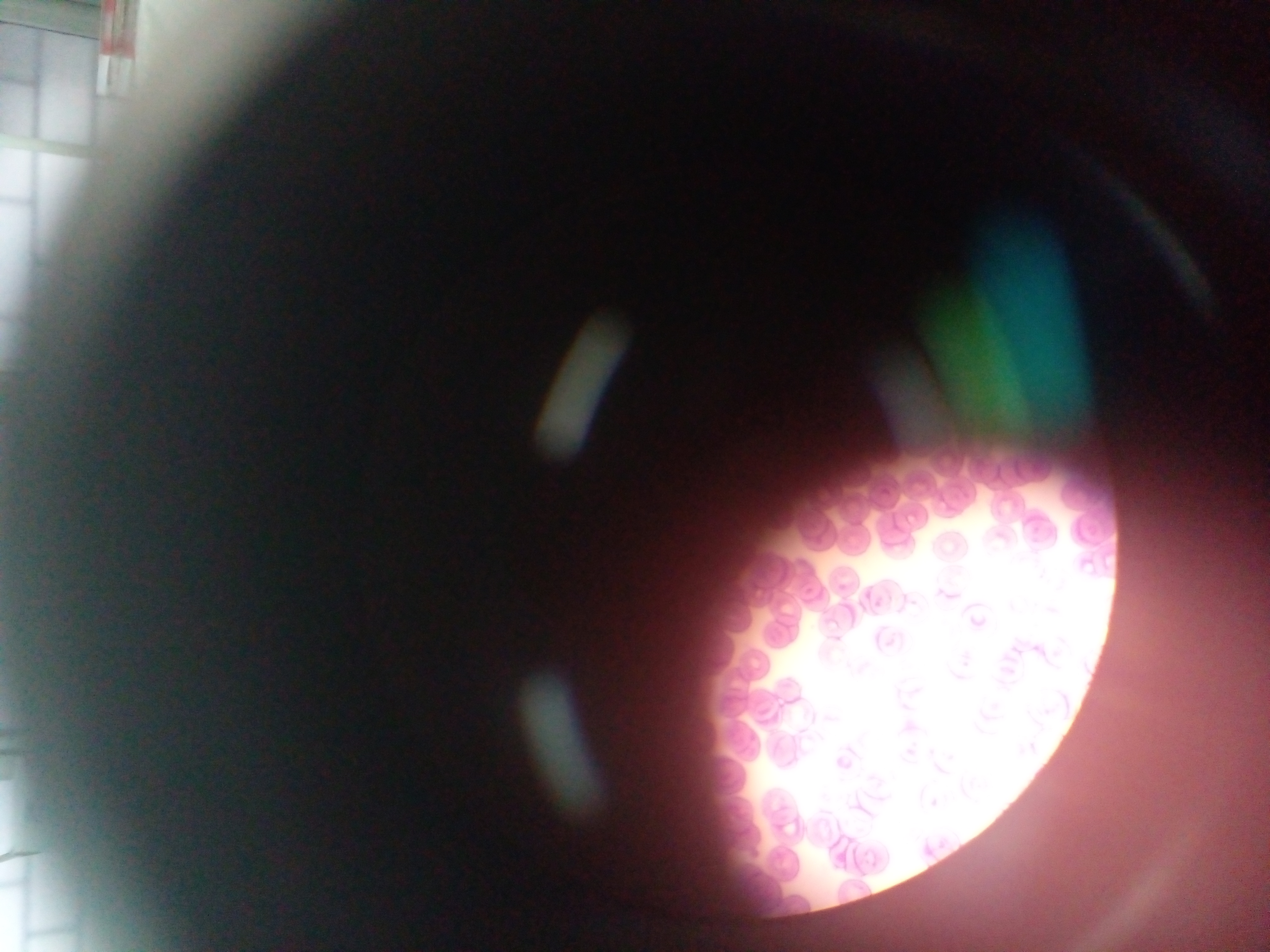
field of view = single
artifact (stain precipitate or debris) locations = approximate bounding boxes as {left, top, right, bottom} in pixels: {91, 0, 148, 74}
image size = 1270×952 pixels
preparation = thin blood film
country = Ghana
capture = mobile-phone photograph through a microscope